Assess this cell for malaria.
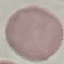
It is uninfected.

Giemsa-stained preparation. Photographed with a smartphone camera at the microscope eyepiece. Automatically extracted cell patch, resized to 64 × 64 pixels. Thin blood film.